Point out each leukocyte.
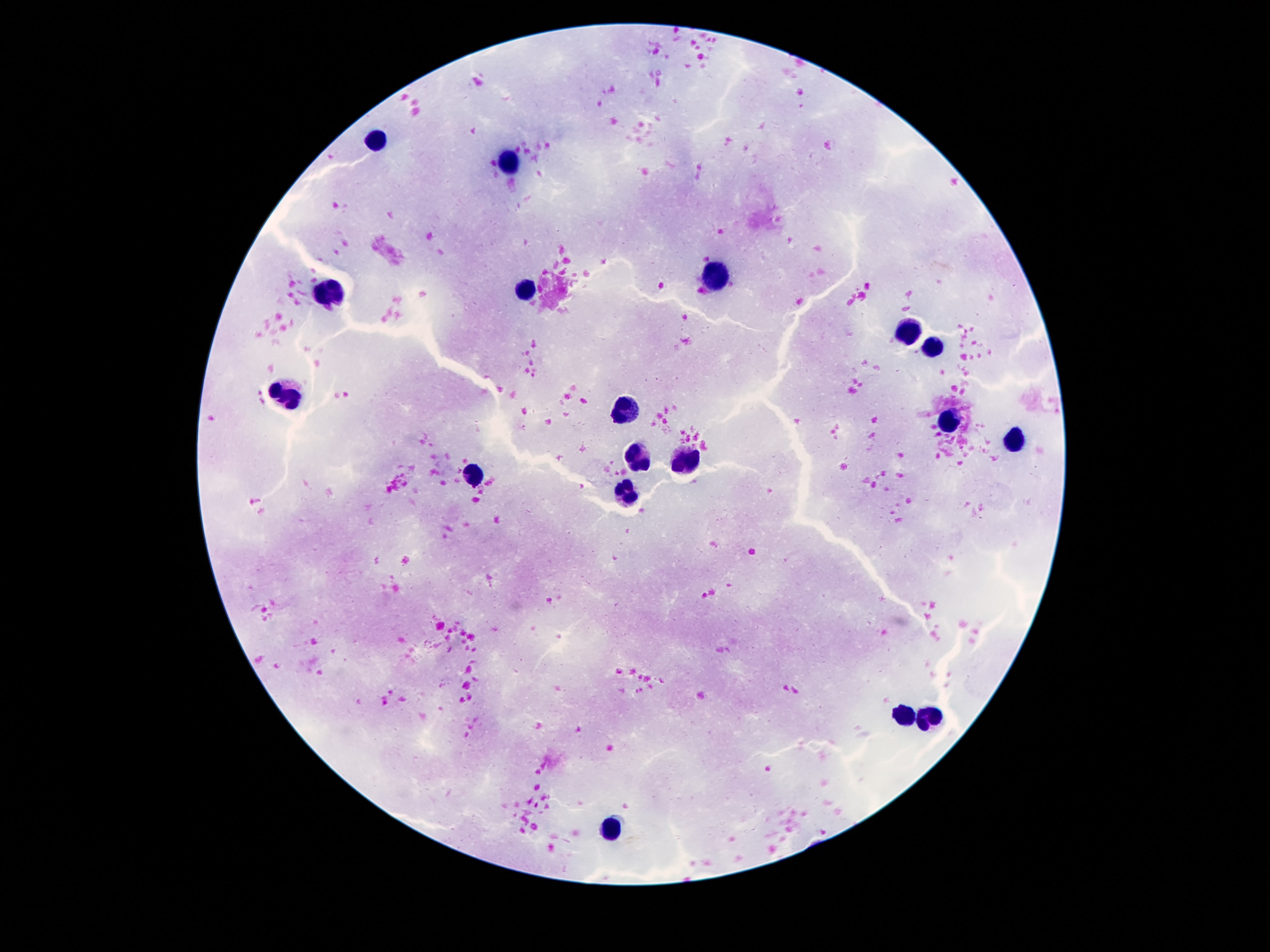
Approximate centers as {x, y} in pixels.
Leukocytes: {376, 138}, {507, 161}, {714, 275}, {526, 292}, {331, 293}, {912, 330}, {928, 349}, {287, 395}, {630, 406}, {946, 424}, {1013, 443}, {637, 458}, {686, 458}, {474, 476}, {627, 494}, {904, 717}, {929, 719}, {612, 827}.

field_of_view: single
patient_malaria_status: not infected
image_size: 1270×952 pixels
capture: smartphone camera through the microscope eyepiece
preparation: thick blood smear
magnification: 100x
stain: Giemsa